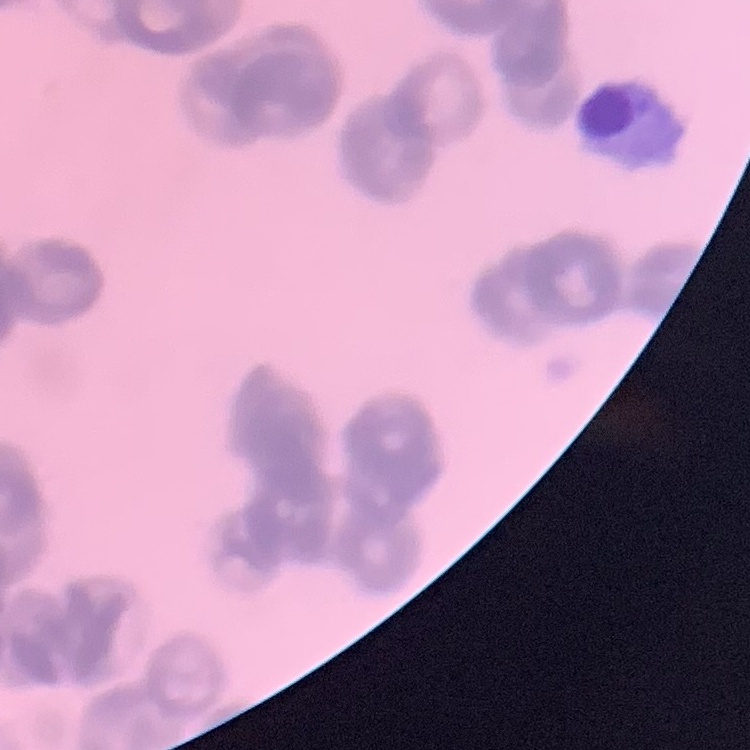
The red blood cells exhibit rouleaux formation. Field's or Giemsa stain. Square crop of a larger photomicrograph. Thin peripheral smear.